State which parasite is depicted.
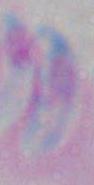

Toxoplasma gondii.

Summary:
  - Magnification: 1000x
  - Modality: micrograph